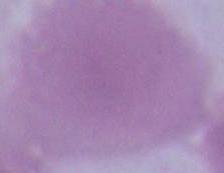
magnification = 1000x
modality = photomicrograph
identification = red blood cell